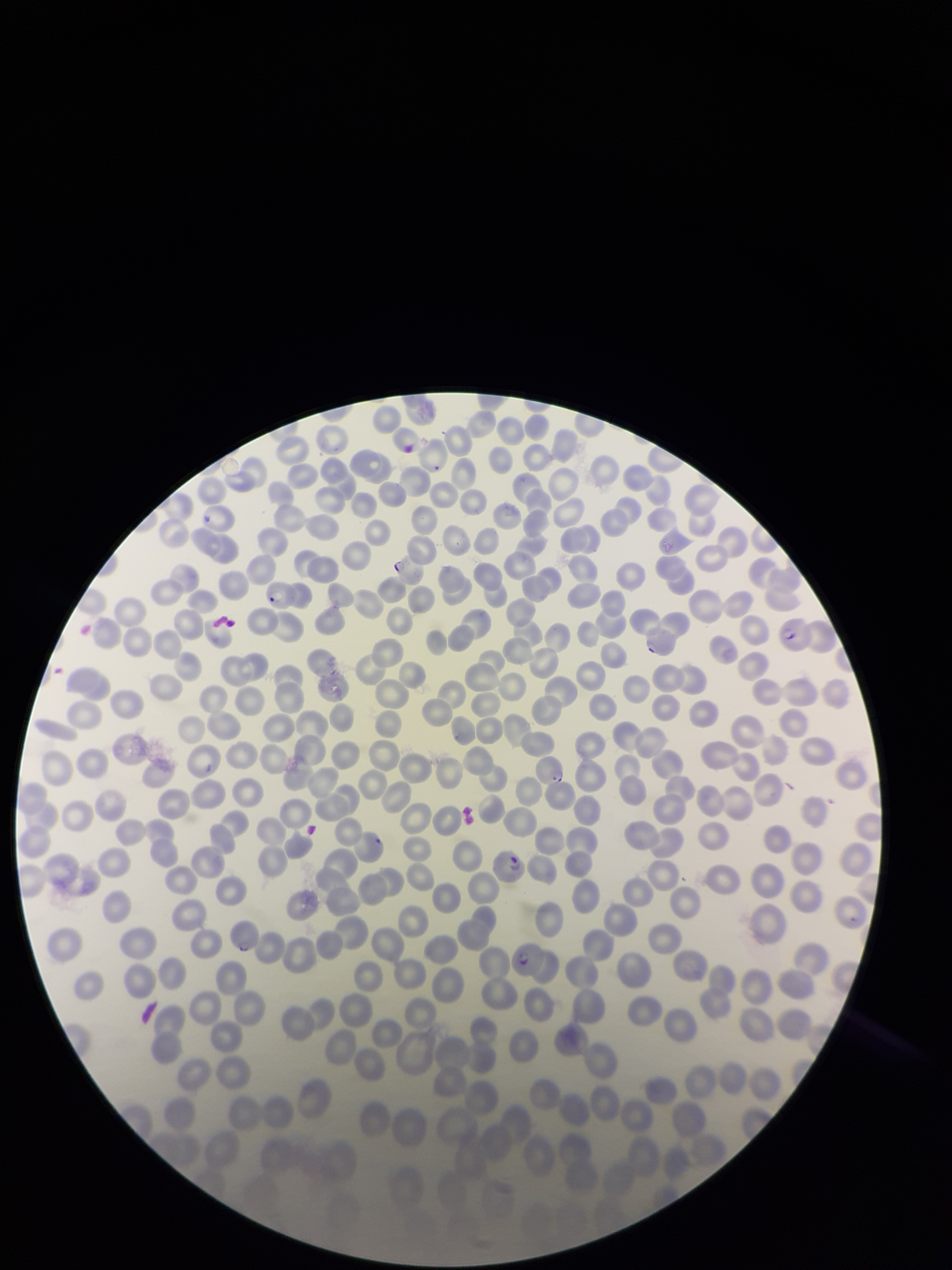
Summary:
  - Image size: 952×1270 pixels
  - Red blood cell count: 153
  - Field of view: one from this slide
  - Parasitized red blood cell count: 5
  - Patient malaria status: positive
  - Species reported for this patient: Plasmodium falciparum
  - Capture: smartphone photograph through the microscope eyepiece
  - Stain: Giemsa
  - Parasitized red blood cells: detected
  - Preparation: thin